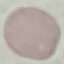
Result: no malaria parasites seen. Photographed with a smartphone camera at the microscope eyepiece. Giemsa stain. Automatically extracted cell patch, resized to 64 × 64 pixels. Thin smear of blood.